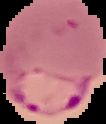

Summary:
  - Image size: 106×124 pixels
  - Image type: segmented cell region with the area outside set to black
  - Result: Plasmodium parasites identified
  - Preparation: thin blood film